Assess the morphology of the erythrocytes.
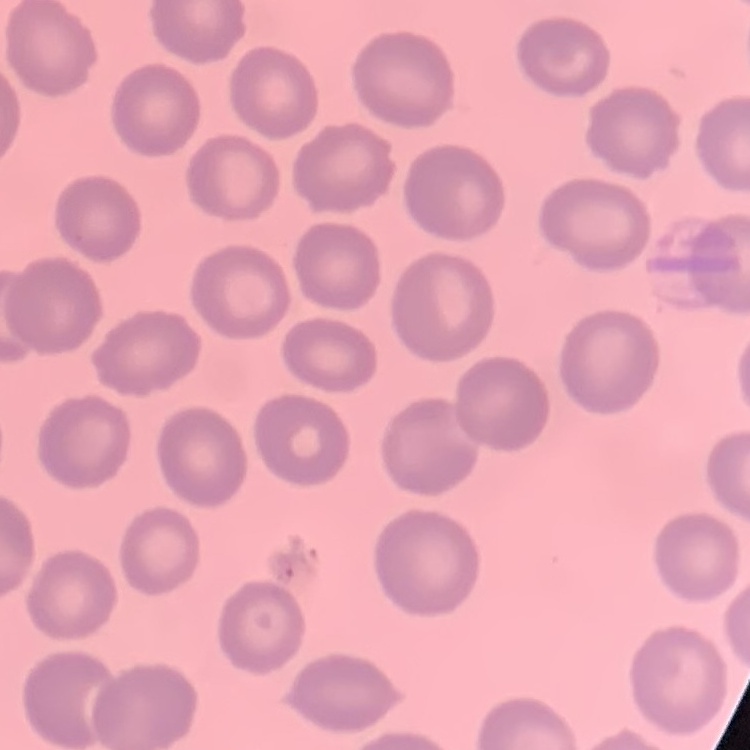

No rouleaux formation.

One tile cut from a larger photomicrograph. Thin blood film. Stained with either Field's or Giemsa.